Identify the parasite.
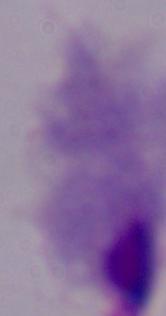
A trichomonad.

{
  "magnification": "1000x",
  "modality": "photomicrograph"
}